State which parasite is depicted.
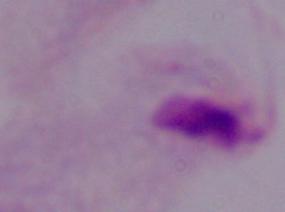

A trichomonad.

{
  "modality": "photomicrograph",
  "magnification": "1000x"
}